Locate every Plasmodium parasite by life-cycle stage, and every leukocyte.
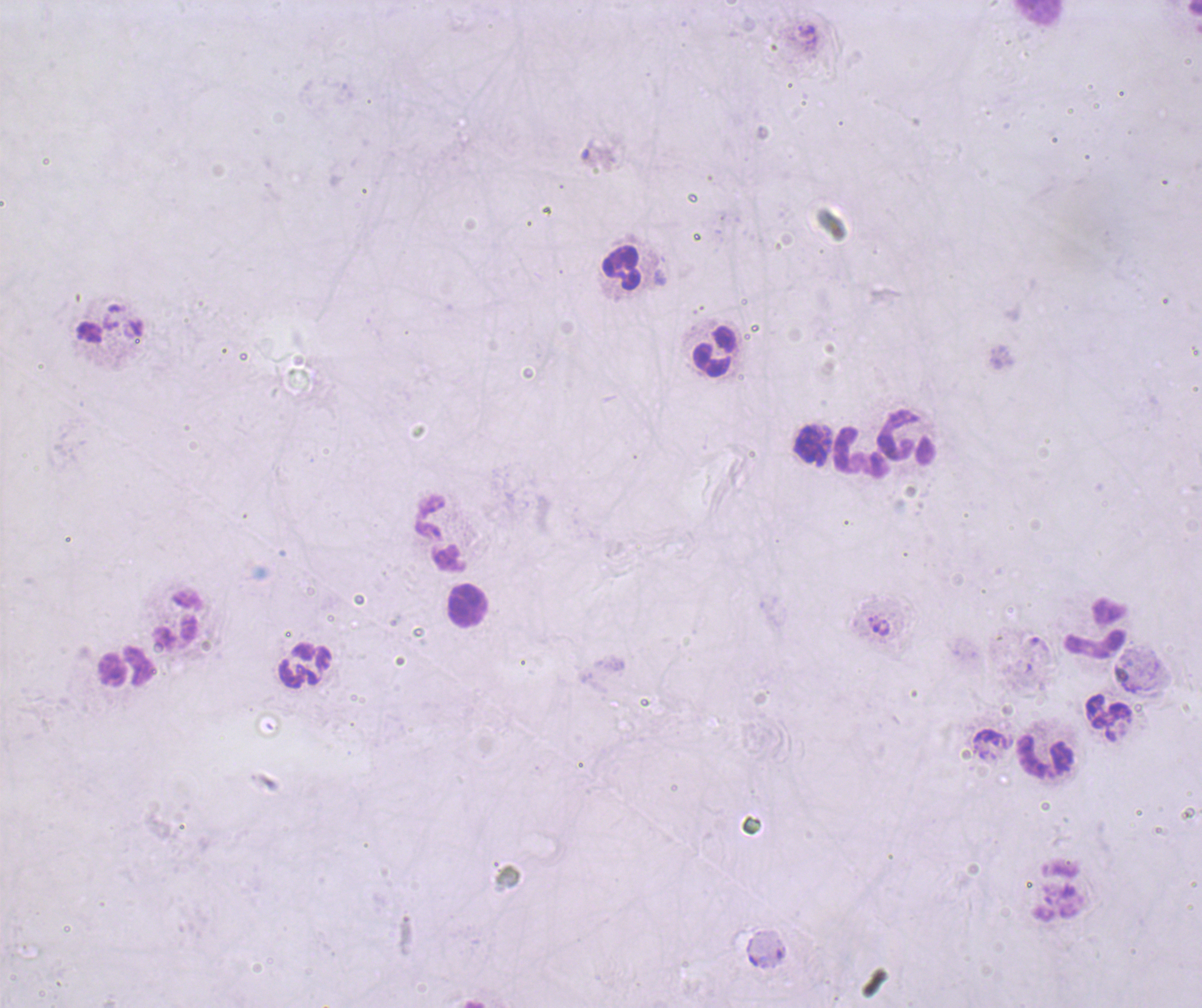

Negative for Plasmodium parasites.
Approximate centers as (x, y) in pixels.
Leukocytes: (620, 266), (712, 351), (906, 437), (810, 447), (862, 452), (441, 533), (468, 605), (178, 618), (1096, 628), (304, 665), (126, 667), (1109, 712), (1044, 755).

context = previously used in a real diagnosis
field of view = single
magnification = 100x
preparation = thick smear of blood
stain = Romanowsky
image size = 1202×1008 pixels
coloration quality = bad
background quality = poor